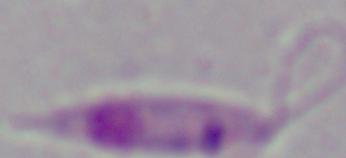

Summary:
  - Magnification: 1000x
  - Modality: micrograph
  - Identification: Leishmania